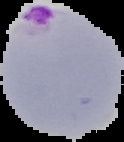
image type = segmented cell region on a black background
image size = 124×142 pixels
result = Plasmodium parasites identified
preparation = thin blood film